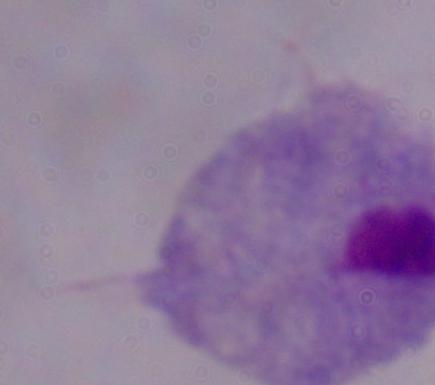 Micrograph. A trichomonad is seen. 1000x magnification.